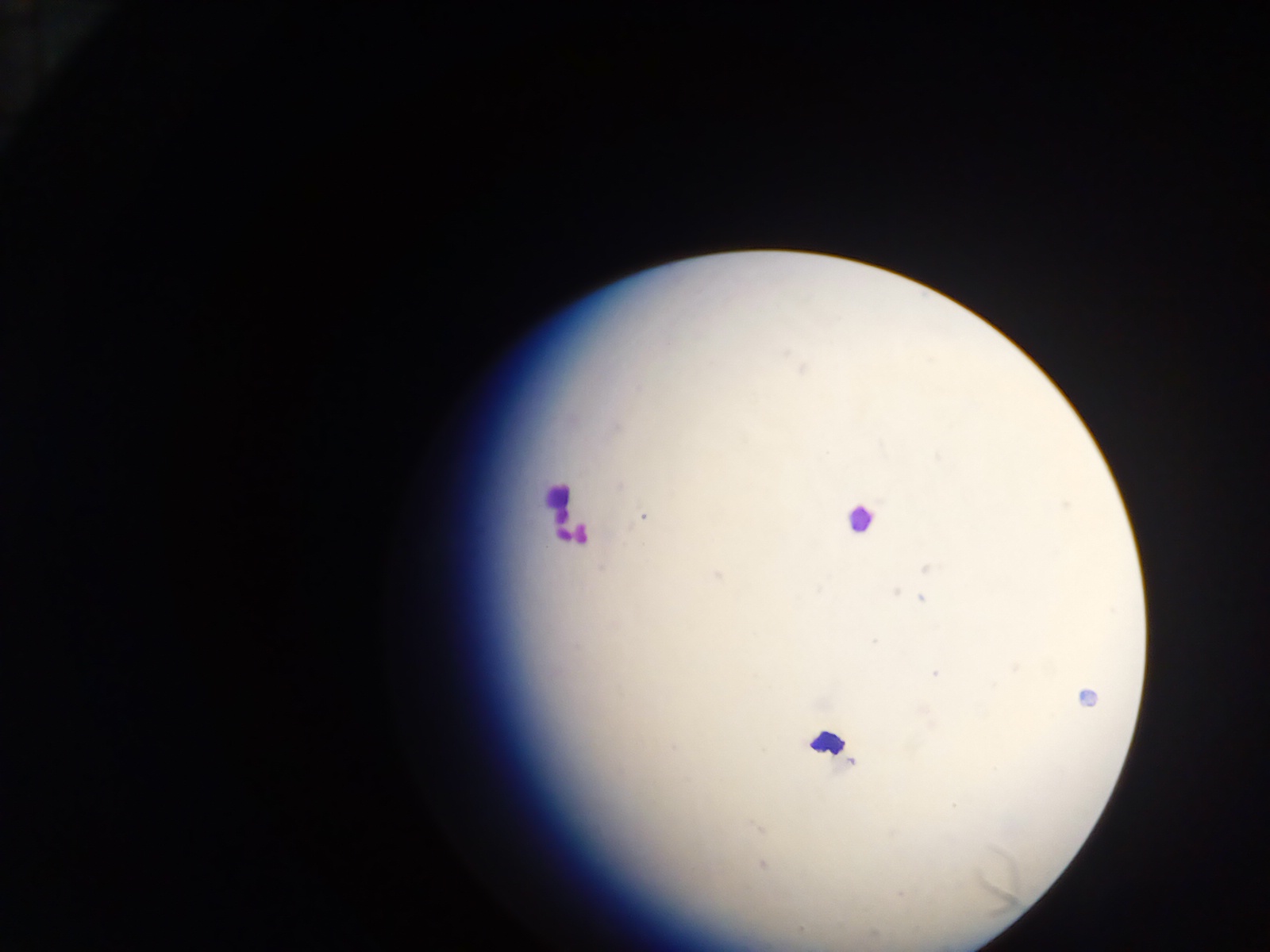
country = Ghana
image size = 1270×952 pixels
leukocyte locations = approximate centers as x y in pixels: 560 507; 859 519; 828 743
capture = mobile-phone photograph through a microscope
malaria parasite locations = approximate centers as x y in pixels: 802 369; 637 387; 616 427; 937 457; 619 486; 643 516; 926 569; 716 575; 819 590; 896 593; 922 598; 874 641; 1016 668; 935 673; 1086 696; 674 746; 952 805; 757 827; 762 864; 901 895; 801 928
preparation = thick blood film
field of view = single